Give a bounding box for every Plasmodium parasite, every leukocyte, and every artifact (stain precipitate or debris).
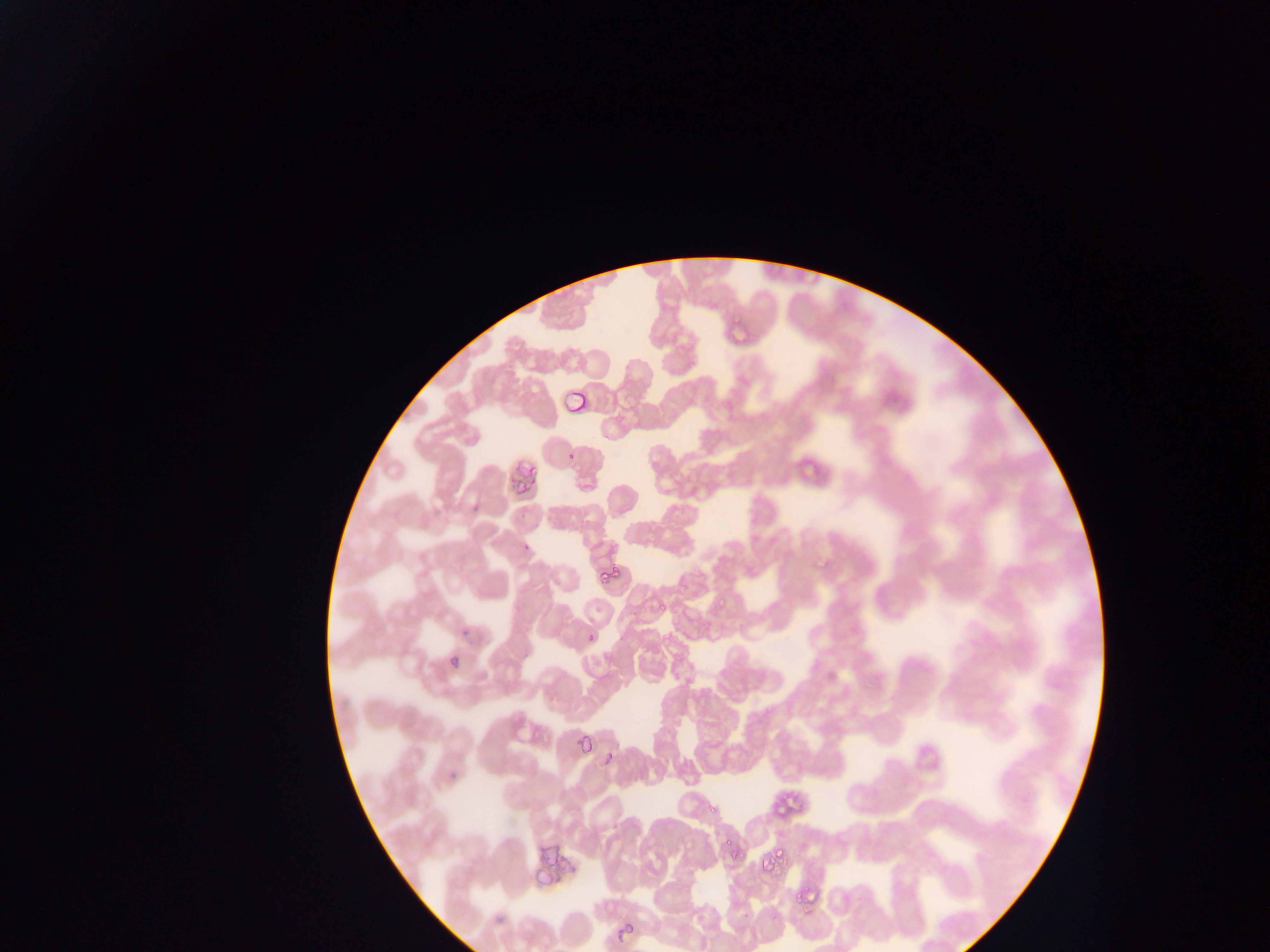

Approximate bounding boxes as (left, top, right, bottom) in pixels.
Plasmodium parasites: (731, 310, 744, 327), (561, 391, 586, 416), (720, 397, 737, 416), (566, 451, 577, 463), (812, 557, 830, 574), (599, 562, 625, 584), (711, 595, 735, 608), (656, 602, 666, 613), (579, 636, 594, 647), (577, 732, 595, 756), (603, 752, 619, 767), (786, 793, 808, 818), (704, 795, 724, 819), (772, 801, 786, 818), (714, 830, 739, 853), (772, 841, 789, 861), (727, 847, 748, 863), (758, 863, 770, 878), (792, 890, 803, 907), (762, 907, 782, 921), (612, 922, 639, 940).
No leukocytes observed.

Collected in Ghana. Image is 1270×952 pixels. Photographed through a microscope with a mobile-phone camera. Thin blood film. One field of view.